Outline platelets.
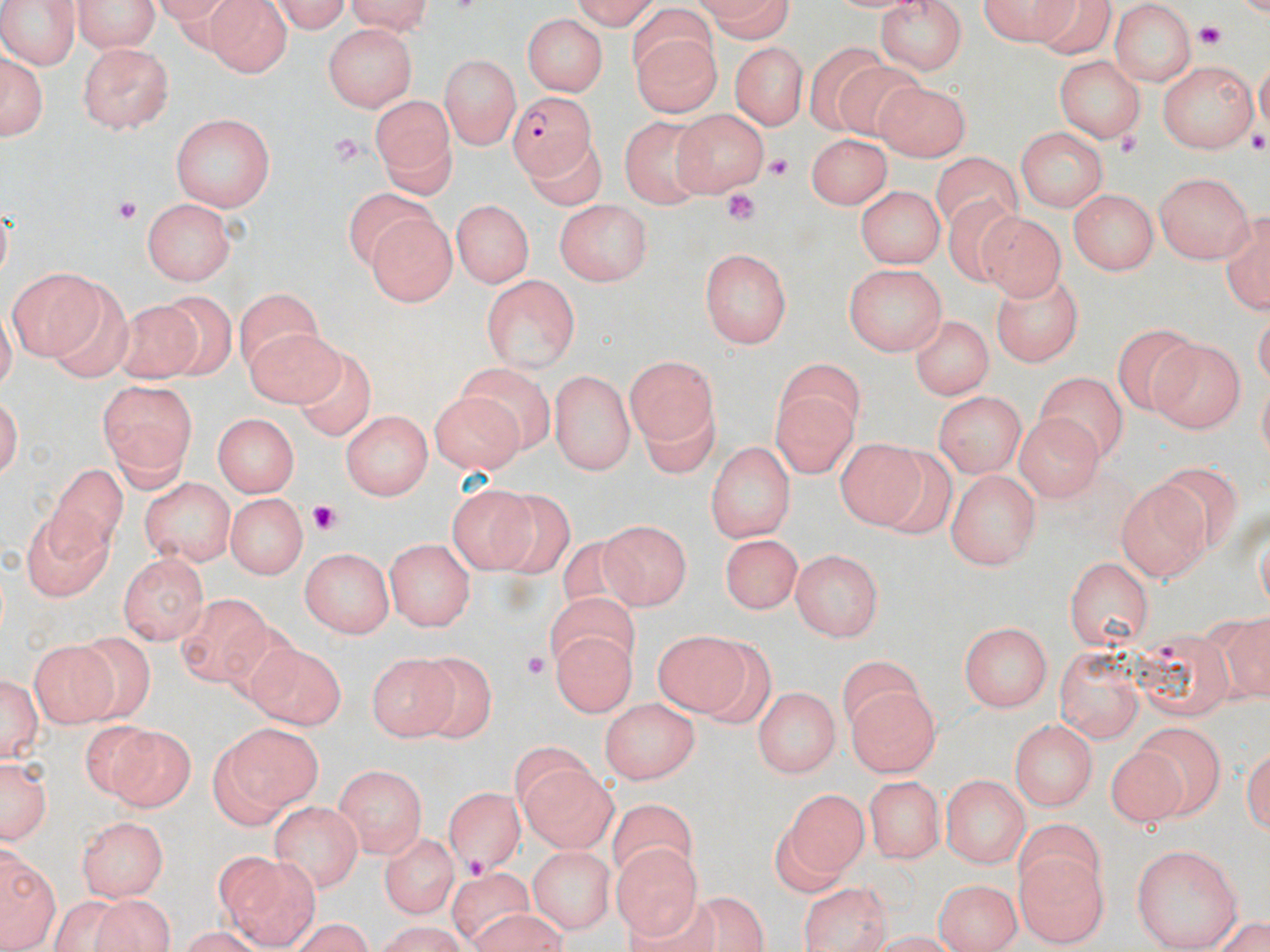

Approximate bounding boxes as (x1,y1)-(x2,y2) corner pairs in pixels.
Platelets: (1195,23)-(1225,49), (1248,131)-(1270,156), (1116,134)-(1142,159), (767,152)-(795,180), (725,192)-(759,225), (114,198)-(139,223), (311,502)-(341,536), (521,648)-(547,679), (463,853)-(490,881).

slide_level_diagnosis: Plasmodium falciparum
uninfected_red_blood_cell_locations: 'approximate bounding boxes as (x1,y1)-(x2,y2) corner pairs in pixels: (0,0)-(84,66), (74,0)-(162,53), (205,0)-(290,78), (261,0)-(351,32), (341,0)-(437,32), (560,0)-(659,28), (690,0)-(797,40), (874,0)-(971,76), (972,2)-(1081,47), (1112,3)-(1196,88), (519,13)-(607,97), (630,21)-(718,117), (323,25)-(412,110), (342,25)-(441,170), (728,41)-(805,132), (807,41)-(891,132), (76,42)-(178,133), (2,46)-(46,143), (437,52)-(521,150), (1053,56)-(1145,142), (1157,60)-(1259,156), (838,66)-(924,137), (872,79)-(971,162), (370,94)-(460,197), (676,106)-(768,193), (172,114)-(274,212), (624,120)-(713,206), (1018,129)-(1106,212), (807,130)-(889,210), (152,133)-(257,281), (519,141)-(604,208), (932,154)-(1023,234), (1152,170)-(1258,262), (856,187)-(942,269), (1069,189)-(1160,275), (346,190)-(435,268), (944,195)-(1026,286), (142,198)-(236,285), (452,198)-(536,290), (554,199)-(652,289), (975,214)-(1063,299), (369,215)-(458,306), (701,248)-(794,350), (5,262)-(103,356), (842,262)-(945,357), (992,272)-(1084,362), (481,273)-(581,374), (44,280)-(137,386), (158,291)-(240,378), (237,293)-(324,370), (109,299)-(203,382), (910,312)-(992,399), (1113,321)-(1194,416), (243,324)-(343,405), (1152,337)-(1244,432), (627,353)-(719,453), (300,354)-(372,440), (782,359)-(867,435), (548,365)-(636,475), (456,366)-(553,450), (1033,371)-(1130,461), (96,376)-(199,486), (932,388)-(1027,476), (774,390)-(853,477), (431,393)-(527,477), (640,403)-(717,480), (340,409)-(433,501), (212,413)-(300,496), (1012,416)-(1107,502), (706,437)-(796,543), (834,437)-(933,535), (45,466)-(127,562), (945,467)-(1038,570), (140,477)-(236,565), (1113,478)-(1209,582), (443,481)-(542,574), (226,492)-(305,578), (484,492)-(574,576), (17,505)-(116,598), (602,518)-(691,610), (716,532)-(801,613), (387,535)-(476,632), (559,537)-(644,619), (300,547)-(394,638), (789,548)-(881,642), (119,551)-(208,644), (1063,555)-(1153,654), (549,593)-(639,672), (180,595)-(274,682), (1227,613)-(1270,702), (961,622)-(1052,712), (549,627)-(639,716), (62,629)-(157,716), (650,629)-(751,719), (1135,630)-(1227,721), (26,638)-(113,728), (242,642)-(347,725), (1054,642)-(1144,742), (363,646)-(467,738), (412,650)-(494,742), (838,660)-(928,736), (1,671)-(43,767), (753,685)-(840,776), (845,686)-(939,778), (602,699)-(700,784), (1010,717)-(1098,812), (94,723)-(194,811), (228,725)-(325,808), (1133,725)-(1226,815), (208,741)-(286,830), (1,752)-(50,844), (1109,752)-(1180,831), (517,754)-(618,854), (333,764)-(427,856), (943,773)-(1028,870), (864,776)-(944,866), (443,784)-(524,875), (789,793)-(861,884), (270,801)-(365,890), (610,806)-(693,881), (76,816)-(169,896), (1010,820)-(1101,894), (377,831)-(456,920), (3,844)-(57,952), (527,844)-(615,934), (1132,844)-(1240,951), (615,845)-(698,939), (1019,850)-(1107,945), (228,858)-(317,945), (451,869)-(535,943), (935,876)-(1020,952), (795,882)-(893,952), (680,895)-(763,952), (92,897)-(169,952), (469,910)-(564,951), (362,922)-(478,952)'
magnification: 1000x
preparation: thin blood film
image_size: 1270×952 pixels
plasmodium_falciparum_infected_red_blood_cell_locations: 'approximate bounding boxes as (x1,y1)-(x2,y2) corner pairs in pixels: (509,91)-(596,178)'
stain: May-Grünwald-Giemsa
modality: light microscopy
field_of_view: single